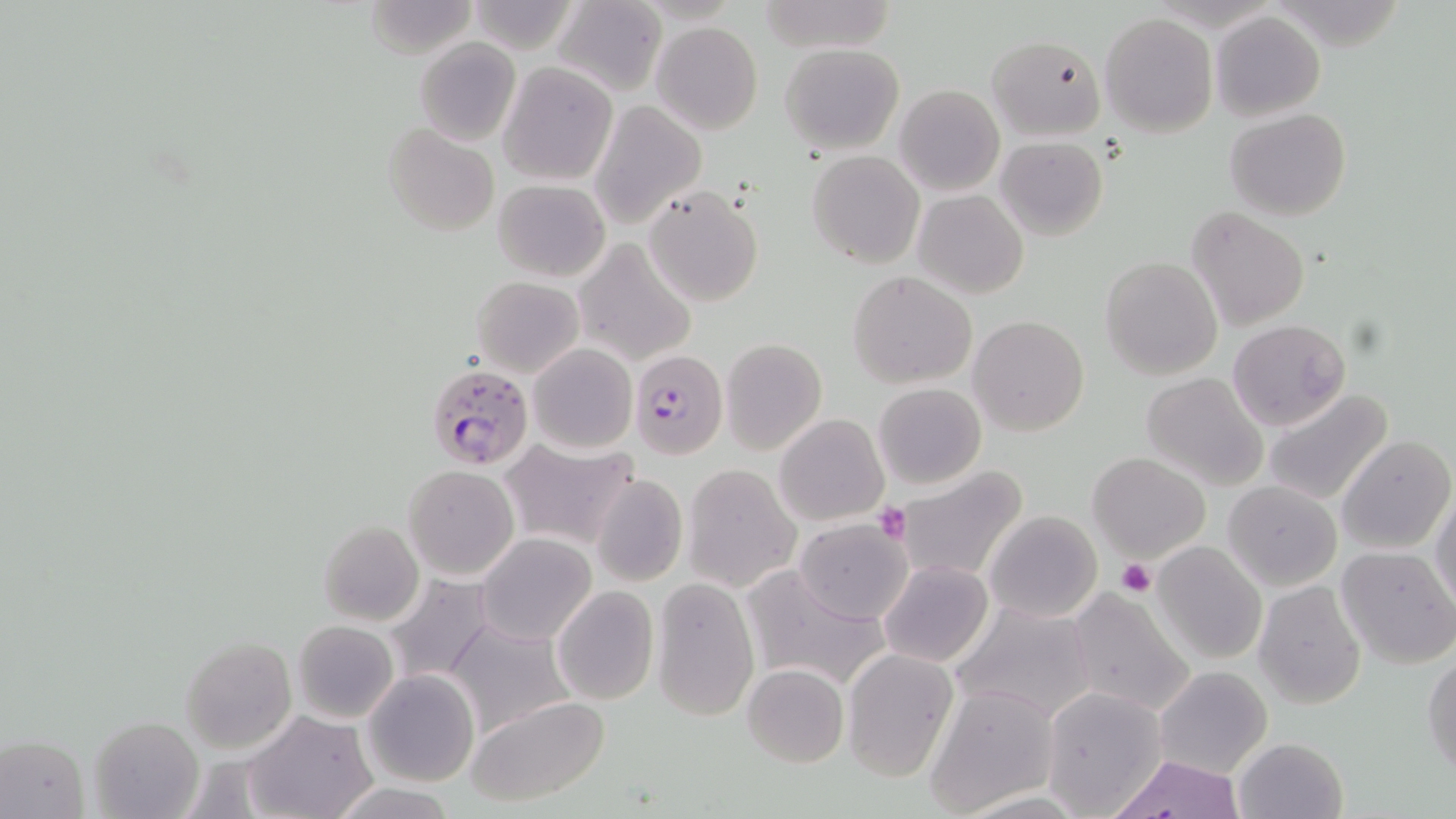
Approximate bounding boxes as [x1, y1, x2, y2] in pixels. Platelet locations: [874, 502, 911, 544], [1117, 559, 1156, 596]. Plasmodium falciparum-infected red blood cell locations: [630, 349, 726, 459], [425, 363, 534, 470]. Uninfected red blood cell locations: [365, 0, 479, 60], [464, 1, 586, 54], [553, 1, 667, 98], [1211, 11, 1326, 121], [1100, 12, 1218, 135], [651, 22, 762, 134], [987, 33, 1107, 139], [413, 38, 521, 146], [780, 43, 904, 153], [499, 62, 617, 185], [895, 84, 1004, 196], [588, 101, 705, 228], [1226, 107, 1350, 222], [385, 122, 499, 236], [994, 134, 1109, 242], [808, 150, 925, 270], [493, 179, 611, 281], [643, 184, 763, 308], [914, 189, 1028, 299], [1188, 208, 1310, 330], [575, 238, 696, 366], [1099, 256, 1223, 380], [848, 270, 978, 389], [471, 275, 585, 379], [968, 316, 1090, 437], [1228, 319, 1351, 431], [721, 338, 827, 454], [527, 343, 637, 454], [1141, 371, 1270, 492], [872, 383, 987, 491], [1263, 387, 1394, 505], [774, 413, 889, 527], [1336, 435, 1455, 555], [500, 440, 637, 549], [1089, 452, 1211, 562], [682, 464, 800, 592], [403, 465, 519, 580], [894, 465, 1031, 586], [590, 473, 688, 588], [1223, 480, 1342, 590], [1430, 491, 1455, 613], [984, 510, 1102, 622], [793, 518, 913, 624], [317, 520, 423, 626], [475, 533, 597, 645], [1151, 540, 1269, 667], [1336, 545, 1456, 668], [879, 561, 993, 668], [738, 564, 886, 693], [381, 573, 498, 687], [651, 578, 760, 719], [1253, 581, 1368, 710], [552, 585, 658, 704], [1065, 587, 1196, 717], [949, 598, 1099, 725], [444, 614, 577, 736], [292, 619, 400, 724], [180, 637, 296, 754], [840, 649, 957, 781], [1423, 652, 1455, 778], [742, 663, 849, 768], [1153, 665, 1272, 779], [363, 670, 480, 788], [925, 684, 1059, 813], [1041, 684, 1167, 816], [464, 694, 610, 807], [245, 711, 375, 819], [89, 716, 203, 819], [1, 734, 88, 818], [1233, 737, 1348, 819], [1108, 754, 1248, 819], [328, 780, 456, 818]. Slide-level diagnosis: Plasmodium falciparum. One field of a larger specimen. Image is 1456×819 pixels. 1000x magnification. Optical microscopy. May-Grünwald-Giemsa-stained preparation. Thin blood film.